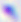

Summary:
  - Magnification: 400x
  - Modality: micrograph
  - Identification: Toxoplasma gondii